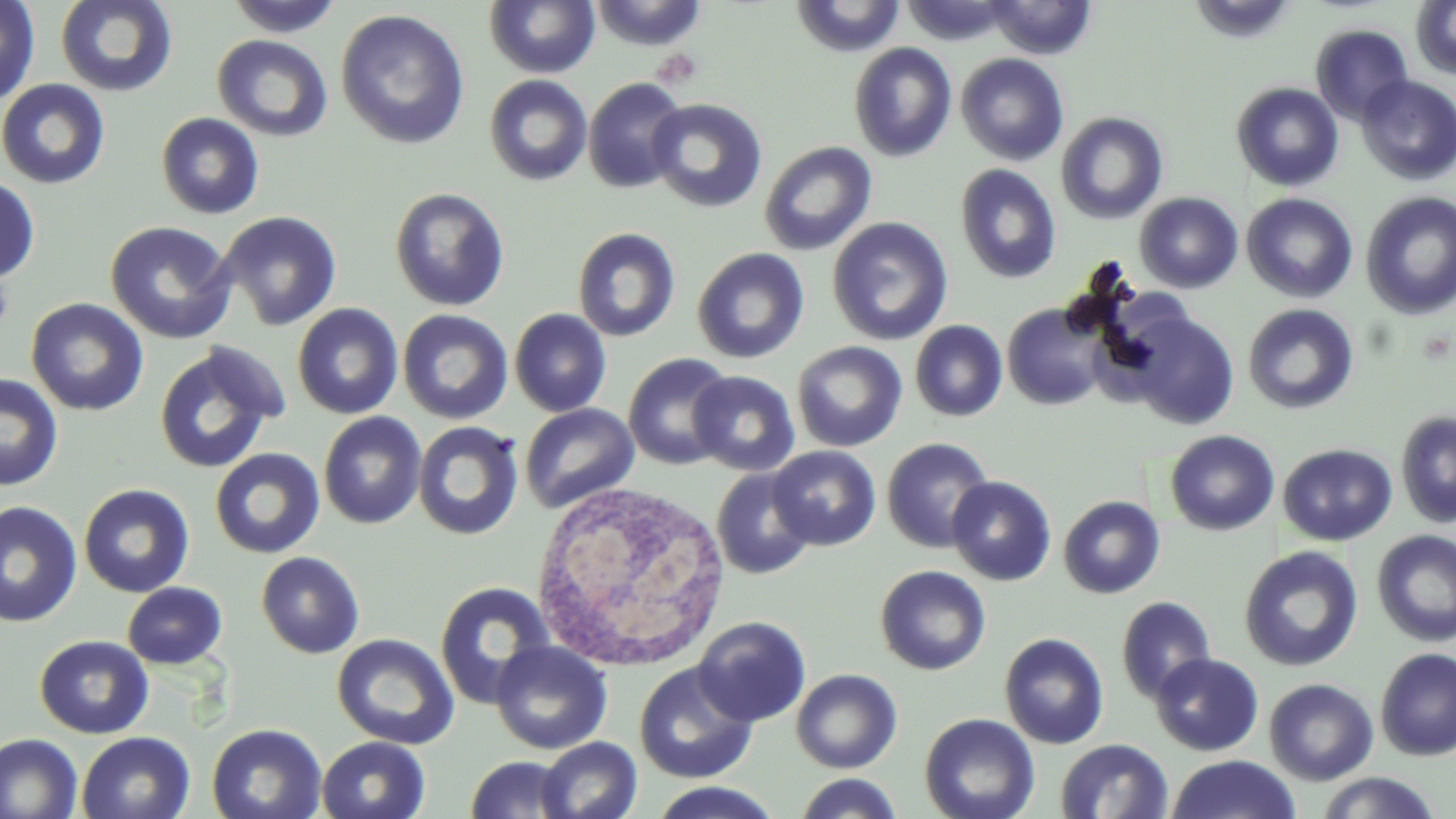

{
  "slide_level_diagnosis": "negative for blood parasites",
  "white_blood_cell_locations": "approximate bounding boxes as named x1/y1/x2/y2 corners in pixels: (x1=529, y1=478, x2=733, y2=673)",
  "image_size": "1456×819 pixels",
  "stain": "May-Grünwald-Giemsa",
  "field_of_view": "one of a larger specimen",
  "platelet_locations": "approximate bounding boxes as named x1/y1/x2/y2 corners in pixels: (x1=0, y1=271, x2=15, y2=336)",
  "preparation": "thin blood smear",
  "modality": "light microscopy",
  "uninfected_red_blood_cell_locations": "approximate bounding boxes as named x1/y1/x2/y2 corners in pixels: (x1=0, y1=0, x2=41, y2=108), (x1=54, y1=0, x2=179, y2=98), (x1=224, y1=0, x2=346, y2=38), (x1=587, y1=0, x2=709, y2=52), (x1=790, y1=0, x2=907, y2=57), (x1=902, y1=0, x2=1013, y2=46), (x1=1187, y1=0, x2=1298, y2=43), (x1=484, y1=1, x2=601, y2=78), (x1=985, y1=1, x2=1097, y2=59), (x1=1411, y1=1, x2=1456, y2=79), (x1=335, y1=8, x2=470, y2=150), (x1=1311, y1=24, x2=1414, y2=125), (x1=212, y1=34, x2=333, y2=142), (x1=848, y1=42, x2=958, y2=162), (x1=955, y1=53, x2=1069, y2=166), (x1=483, y1=74, x2=593, y2=186), (x1=1356, y1=75, x2=1456, y2=185), (x1=583, y1=78, x2=689, y2=194), (x1=0, y1=79, x2=110, y2=189), (x1=1230, y1=82, x2=1344, y2=192), (x1=646, y1=98, x2=768, y2=213), (x1=1055, y1=111, x2=1169, y2=225), (x1=156, y1=112, x2=265, y2=219), (x1=759, y1=140, x2=878, y2=256), (x1=954, y1=164, x2=1062, y2=284), (x1=0, y1=173, x2=40, y2=285), (x1=389, y1=187, x2=510, y2=311), (x1=1360, y1=191, x2=1456, y2=320), (x1=1134, y1=192, x2=1243, y2=293), (x1=1241, y1=193, x2=1358, y2=303), (x1=217, y1=210, x2=342, y2=331), (x1=827, y1=216, x2=954, y2=346), (x1=105, y1=221, x2=237, y2=344), (x1=572, y1=227, x2=681, y2=343), (x1=692, y1=248, x2=809, y2=364), (x1=26, y1=298, x2=149, y2=416), (x1=292, y1=303, x2=403, y2=419), (x1=1002, y1=303, x2=1109, y2=410), (x1=1243, y1=303, x2=1359, y2=415), (x1=397, y1=308, x2=513, y2=425), (x1=509, y1=308, x2=612, y2=417), (x1=1121, y1=309, x2=1241, y2=430), (x1=909, y1=320, x2=1008, y2=421), (x1=792, y1=341, x2=907, y2=452), (x1=152, y1=343, x2=286, y2=474), (x1=623, y1=352, x2=735, y2=470), (x1=688, y1=370, x2=801, y2=476), (x1=0, y1=372, x2=64, y2=491), (x1=519, y1=403, x2=639, y2=514), (x1=1396, y1=410, x2=1456, y2=528), (x1=318, y1=411, x2=427, y2=529), (x1=413, y1=421, x2=524, y2=540), (x1=1165, y1=430, x2=1280, y2=536), (x1=881, y1=437, x2=996, y2=553), (x1=1278, y1=444, x2=1397, y2=546), (x1=768, y1=446, x2=881, y2=550), (x1=210, y1=448, x2=326, y2=559), (x1=711, y1=468, x2=816, y2=580), (x1=947, y1=476, x2=1056, y2=585), (x1=78, y1=483, x2=195, y2=597), (x1=1058, y1=495, x2=1165, y2=599), (x1=0, y1=500, x2=82, y2=628), (x1=1372, y1=529, x2=1456, y2=648), (x1=1239, y1=547, x2=1362, y2=671), (x1=256, y1=551, x2=365, y2=658), (x1=875, y1=565, x2=991, y2=675), (x1=435, y1=581, x2=557, y2=708), (x1=122, y1=582, x2=228, y2=670), (x1=1115, y1=596, x2=1217, y2=704), (x1=693, y1=616, x2=811, y2=726), (x1=1000, y1=633, x2=1109, y2=749), (x1=34, y1=634, x2=154, y2=739), (x1=332, y1=634, x2=459, y2=750), (x1=490, y1=641, x2=612, y2=755), (x1=1375, y1=648, x2=1456, y2=760), (x1=1150, y1=652, x2=1264, y2=756), (x1=633, y1=662, x2=758, y2=783), (x1=1149, y1=666, x2=1381, y2=764), (x1=791, y1=668, x2=902, y2=774), (x1=1264, y1=678, x2=1378, y2=785), (x1=919, y1=712, x2=1040, y2=819), (x1=206, y1=723, x2=327, y2=819), (x1=76, y1=731, x2=196, y2=819), (x1=0, y1=733, x2=83, y2=819), (x1=316, y1=736, x2=431, y2=819), (x1=536, y1=736, x2=642, y2=819), (x1=1055, y1=738, x2=1174, y2=819), (x1=463, y1=755, x2=578, y2=818), (x1=1166, y1=755, x2=1301, y2=818), (x1=1314, y1=771, x2=1441, y2=818), (x1=794, y1=773, x2=904, y2=819), (x1=647, y1=782, x2=784, y2=817)",
  "magnification": "1000x"
}